Assess the morphology of the red blood cells.
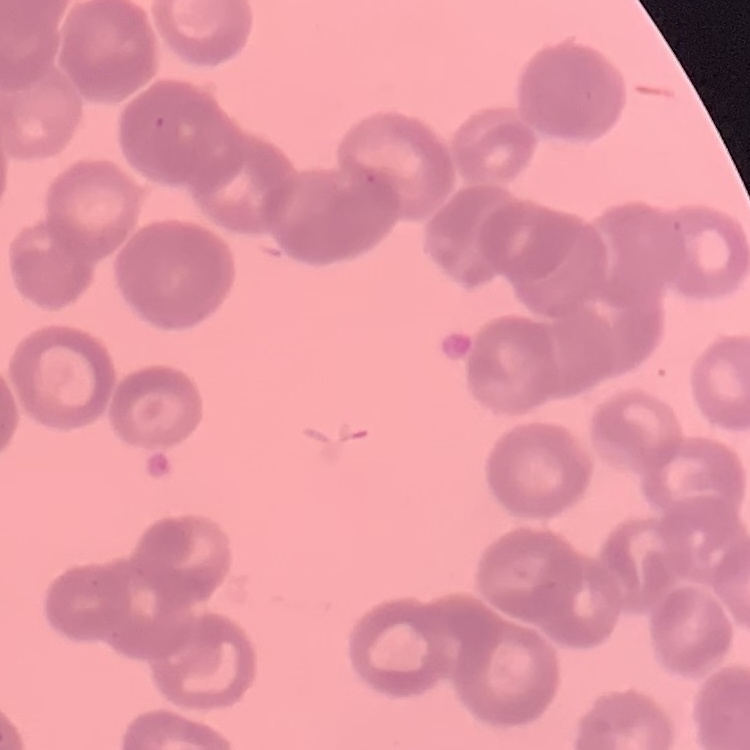
They show rouleaux formation.

Summary:
  - Stain: Field's or Giemsa
  - Image type: one tile cut from a larger photomicrograph
  - Preparation: thin blood film